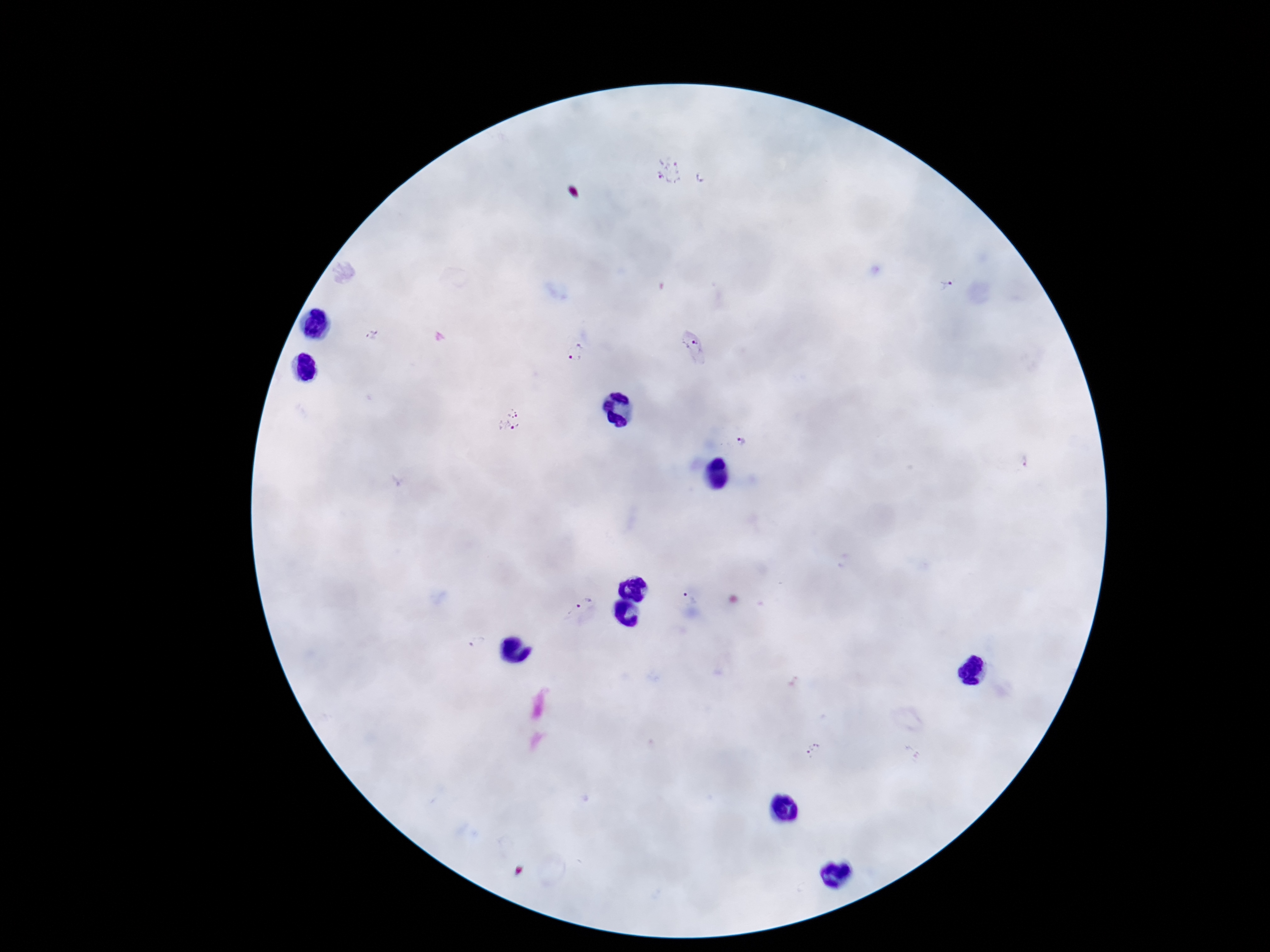

Approximate centers as {x, y} in pixels. Plasmodium parasite locations: {669, 171}, {703, 178}, {947, 286}, {577, 352}, {507, 421}, {743, 442}, {689, 600}, {581, 606}, {479, 644}, {815, 751}. Photographed through the microscope eyepiece with a smartphone camera. Image is 1270×952 pixels. Giemsa-stained preparation. 100x magnification. Thick peripheral-blood smear. One field from this slide. Patient malaria status: positive.